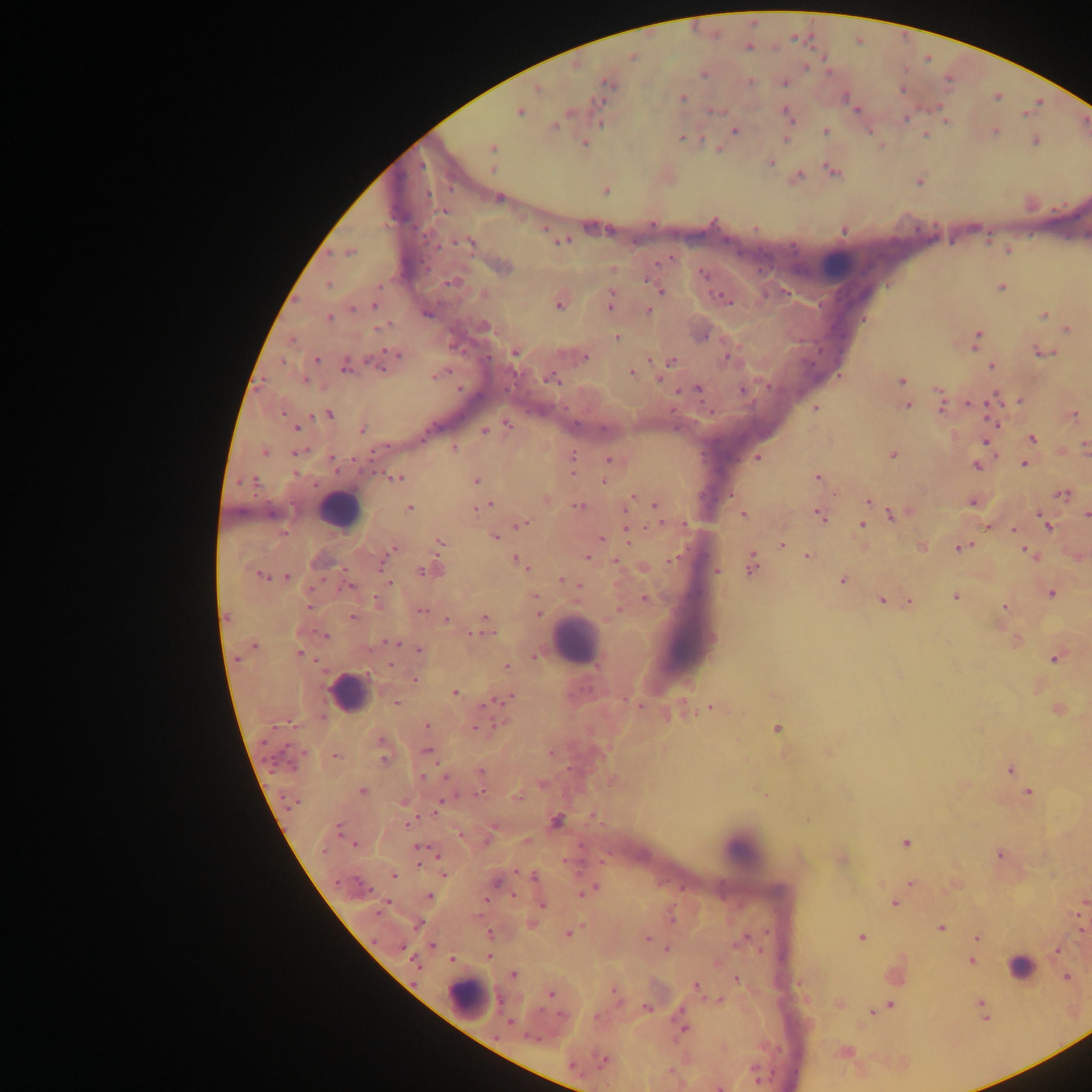

Approximate centers as (x, y) in pixels.
Summary:
  - Plasmodium parasite locations: (748, 46), (633, 57), (704, 74), (607, 82), (783, 82), (536, 87), (902, 89), (683, 98), (856, 109), (716, 111), (519, 112), (787, 114), (906, 118), (945, 120), (554, 126), (734, 130), (995, 131), (825, 132), (924, 134), (682, 138), (786, 138), (1035, 140), (583, 143), (492, 148), (718, 148), (771, 161), (492, 168), (832, 171), (796, 177), (919, 180), (605, 191), (498, 197), (545, 229), (843, 229), (562, 241), (470, 243), (1007, 249), (349, 251), (501, 266), (611, 268), (703, 274), (453, 282), (328, 285), (1001, 287), (660, 290), (483, 293), (723, 297), (559, 301), (610, 302), (375, 305), (648, 310), (1044, 315), (328, 318), (1067, 329), (616, 337), (976, 339), (1042, 350), (514, 352), (395, 356), (583, 357), (727, 357), (388, 358), (316, 359), (671, 361), (345, 366), (992, 366), (631, 373), (435, 375), (551, 378), (658, 378), (901, 380), (697, 388), (680, 390), (1021, 400), (942, 402), (990, 402), (907, 405), (814, 408), (328, 413), (1072, 414), (507, 425), (296, 427), (361, 430), (484, 430), (1032, 438), (986, 440), (1085, 445), (454, 447), (297, 451), (264, 452), (892, 454), (757, 457), (608, 459), (1024, 463), (976, 465), (572, 466), (816, 476), (395, 477), (476, 480), (603, 481), (1062, 493), (634, 495), (545, 499), (868, 500), (972, 500), (488, 503), (654, 504), (578, 506), (409, 509), (744, 514), (864, 514), (893, 514), (820, 515), (1086, 515), (522, 523), (862, 523), (1046, 523), (989, 525), (627, 529), (1013, 529), (494, 536), (600, 538), (440, 543), (781, 544), (922, 546), (961, 547), (392, 549), (1028, 552), (587, 556), (807, 556), (1079, 556), (615, 561), (520, 562), (751, 564), (643, 568), (429, 569), (715, 571), (261, 575), (286, 577), (842, 579), (566, 581), (388, 582), (575, 583), (1051, 593), (955, 596), (645, 598), (881, 600), (378, 601), (909, 602), (1004, 606), (537, 607), (421, 611), (352, 618), (447, 619), (484, 625), (325, 635), (1015, 640), (390, 643), (254, 646), (419, 649), (298, 653), (536, 656), (1056, 656), (506, 667), (414, 680), (454, 692), (502, 699), (396, 702), (711, 707), (1058, 709), (670, 714), (427, 726), (475, 727), (776, 727), (382, 747), (427, 751), (827, 752), (334, 756), (1009, 769), (480, 773), (542, 784), (362, 791), (1028, 793), (404, 801), (555, 820), (408, 823), (338, 828), (489, 837), (527, 841), (905, 842), (354, 844), (418, 849), (999, 854), (841, 859), (444, 874), (394, 875), (534, 876), (496, 882), (910, 882), (953, 885), (589, 889), (428, 896), (512, 896), (541, 902), (894, 902), (1083, 902), (670, 917), (531, 923), (418, 924), (940, 927), (1081, 930), (489, 933), (568, 933), (860, 937), (744, 938), (977, 938), (645, 939), (433, 945), (667, 948), (1057, 950), (489, 956), (452, 959), (971, 960), (514, 974), (1066, 976), (735, 978), (696, 986), (551, 993), (615, 995), (718, 1001), (979, 1003), (839, 1004), (890, 1005), (647, 1008), (872, 1012), (683, 1027), (844, 1052), (602, 1060), (757, 1077), (720, 1086)
  - Leukocyte locations: (836, 264), (337, 510), (575, 641), (348, 693), (741, 849), (1021, 967), (468, 998)
  - Field of view: single
  - Preparation: thick blood film
  - Image size: 1092×1092 pixels
  - Country: Ghana
  - Capture: mobile-phone photograph through a microscope